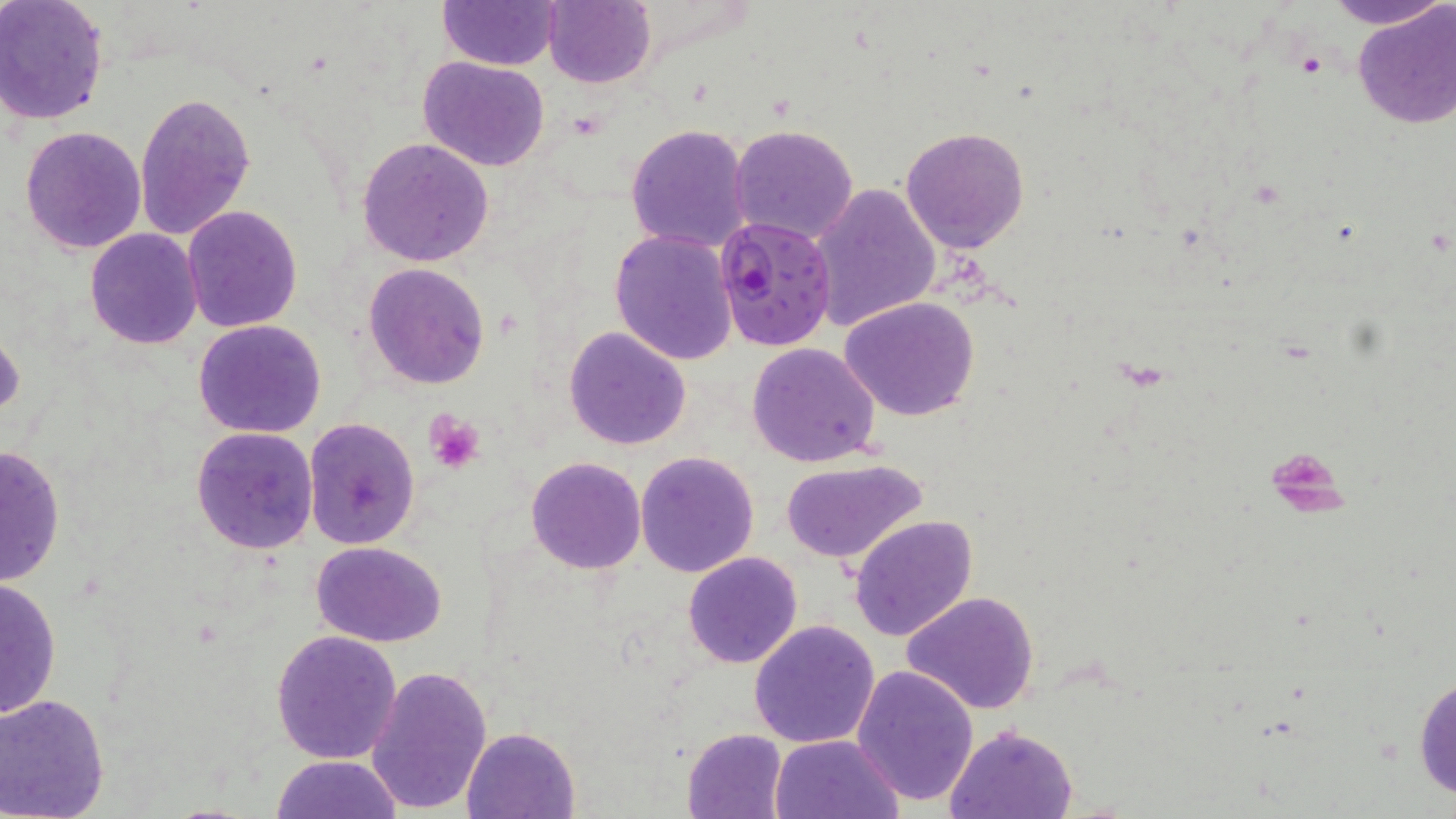
slide_level_diagnosis: Plasmodium falciparum
field_of_view: one of a larger specimen
magnification: 1000x
uninfected_red_blood_cell_locations: 'approximate bounding boxes as [x1, y1, x2, y2] in pixels: [0, 0, 110, 126], [1319, 0, 1451, 28], [439, 1, 559, 69], [543, 1, 656, 88], [1352, 1, 1456, 130], [419, 56, 549, 170], [134, 90, 256, 240], [625, 122, 751, 253], [729, 123, 860, 245], [19, 125, 147, 254], [901, 128, 1029, 254], [357, 138, 494, 266], [810, 183, 941, 332], [183, 205, 302, 332], [84, 228, 201, 349], [610, 229, 737, 366], [364, 263, 490, 388], [840, 297, 982, 423], [195, 319, 328, 438], [564, 327, 691, 449], [0, 328, 23, 423], [747, 342, 881, 467], [302, 416, 421, 551], [191, 426, 319, 554], [0, 444, 67, 584], [636, 452, 759, 576], [527, 457, 645, 573], [781, 462, 925, 564], [850, 515, 978, 643], [312, 541, 446, 647], [682, 551, 802, 669], [0, 575, 61, 721], [902, 591, 1041, 714], [750, 619, 880, 749], [271, 628, 403, 763], [851, 663, 980, 805], [367, 666, 493, 814], [1414, 670, 1455, 805], [0, 693, 111, 819], [946, 723, 1077, 817], [462, 725, 582, 818], [682, 727, 790, 819], [770, 733, 906, 819], [270, 754, 404, 818]'
preparation: thin blood film
stain: May-Grünwald-Giemsa
platelet_locations: 'approximate bounding boxes as [x1, y1, x2, y2] in pixels: [425, 410, 485, 473]'
image_size: 1456×819 pixels
modality: optical microscopy
plasmodium_falciparum_infected_red_blood_cell_locations: 'approximate bounding boxes as [x1, y1, x2, y2] in pixels: [715, 217, 837, 352]'